Outline each Plasmodium falciparum-infected red blood cell.
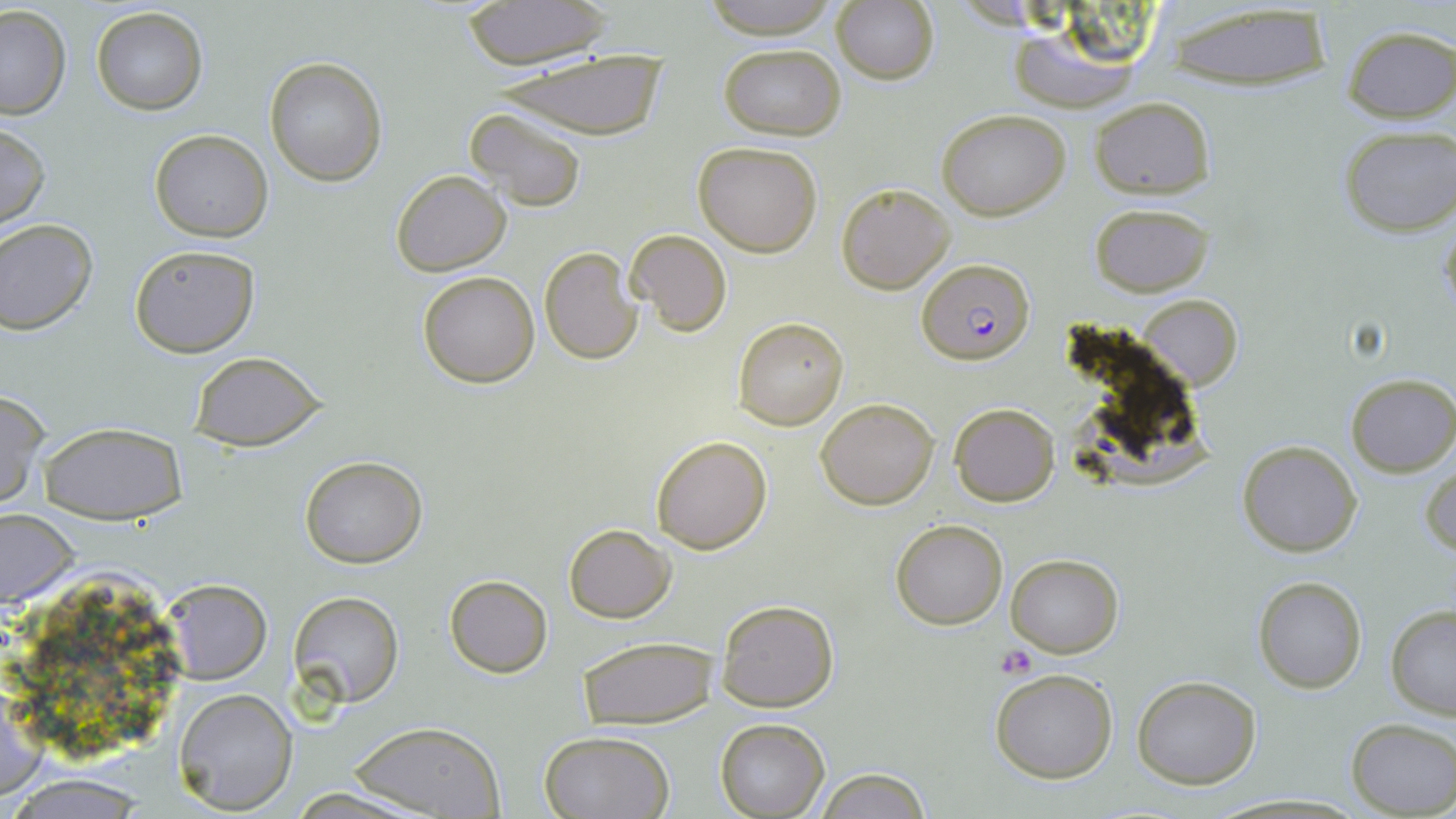
Approximate bounding boxes as (x1,y1)-(x2,y2) corner pairs in pixels.
Plasmodium falciparum-infected red blood cells: (917,259)-(1035,364).

Summary:
  - Platelet locations: (995,644)-(1038,678)
  - Uninfected red blood cell locations: (694,0)-(844,39), (461,1)-(613,70), (831,3)-(939,85), (1165,3)-(1335,92), (91,5)-(209,114), (0,6)-(72,120), (1004,22)-(1143,113), (1341,26)-(1456,122), (719,43)-(846,141), (488,48)-(673,144), (264,57)-(387,185), (1089,97)-(1216,199), (464,108)-(588,213), (937,108)-(1071,220), (0,121)-(50,235), (1339,127)-(1454,237), (149,130)-(273,242), (694,140)-(823,257), (390,170)-(511,276), (836,181)-(956,294), (1088,203)-(1213,296), (0,218)-(98,335), (626,228)-(731,337), (128,243)-(260,356), (540,246)-(642,365), (417,271)-(540,388), (1138,295)-(1241,389), (734,316)-(849,431), (189,352)-(328,451), (1346,373)-(1456,477), (0,391)-(48,508), (816,397)-(940,510), (949,402)-(1061,507), (38,421)-(188,523), (649,434)-(774,554), (1237,439)-(1363,556), (299,457)-(427,568), (1421,464)-(1455,559), (0,506)-(79,610), (891,519)-(1007,630), (563,523)-(676,623), (1005,553)-(1124,657), (444,574)-(553,677), (1253,575)-(1367,694), (161,579)-(273,684), (288,590)-(404,707), (716,599)-(838,712), (1386,604)-(1456,718), (576,636)-(717,730), (990,669)-(1118,784), (1132,676)-(1261,789), (173,687)-(298,815), (715,717)-(829,817), (1346,718)-(1455,817), (347,720)-(505,819), (538,730)-(676,818), (814,767)-(931,819), (0,772)-(158,818), (286,786)-(428,819)
  - Slide-level diagnosis: Plasmodium falciparum
  - Stain: May-Grünwald-Giemsa
  - Preparation: thin blood smear
  - Field of view: single
  - Image size: 1456×819 pixels
  - Modality: optical microscopy
  - Magnification: 1000x